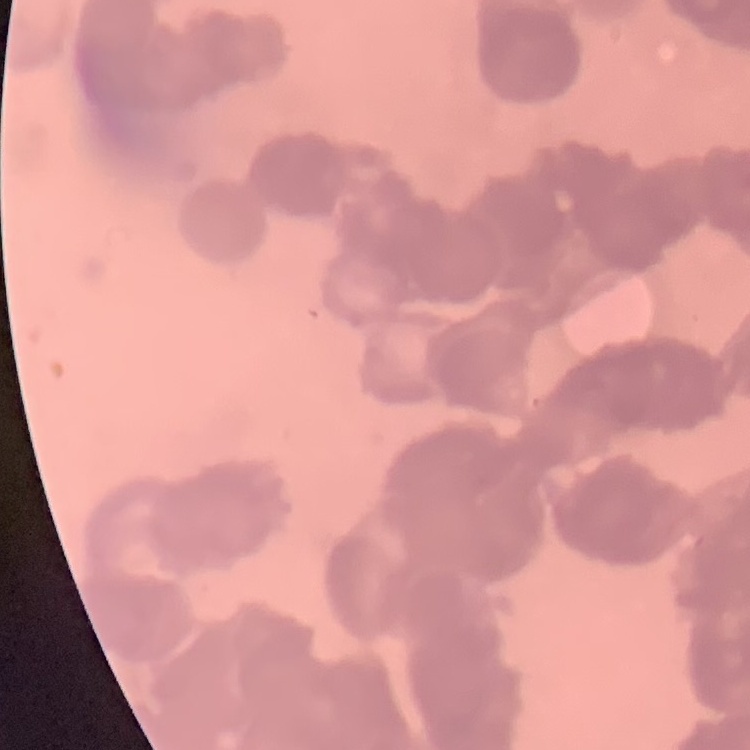
Summary:
  - Erythrocyte morphology: rouleaux formation
  - Image type: square crop of a larger photomicrograph
  - Stain: Field's or Giemsa
  - Preparation: thin peripheral smear